Describe the morphology of the red blood cells.
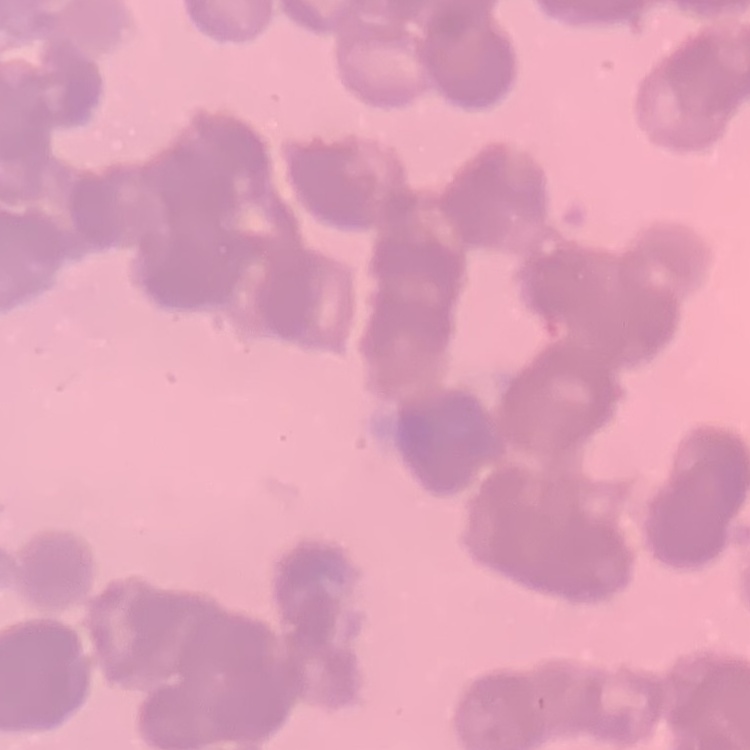
Rouleaux formation.

image type = square crop of a larger photomicrograph
preparation = thin peripheral smear
stain = Field's or Giemsa